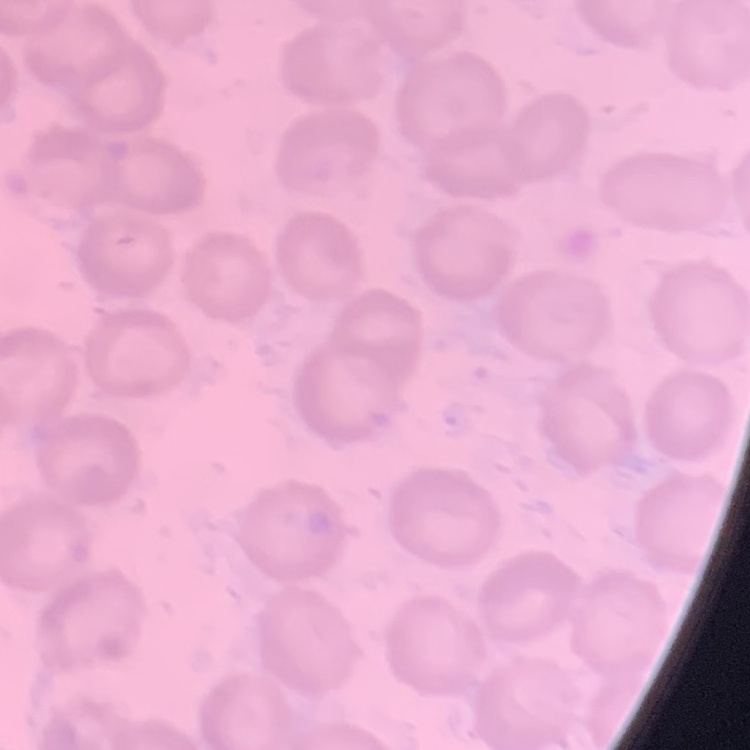
erythrocyte_morphology: no rouleaux formation
stain: Field's or Giemsa
preparation: thin blood film
image_type: square crop of a larger photomicrograph